Point out leukocytes.
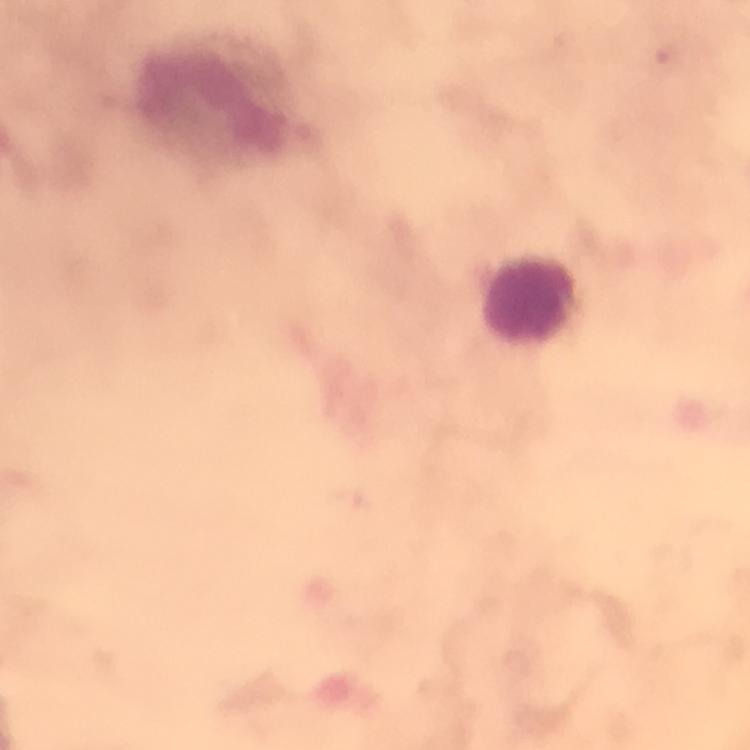

Approximate centers as (x, y) in pixels.
Leukocytes: (216, 103), (530, 301).

Summary:
  - Context: from a diagnostic examination for malaria
  - Plasmodium parasites: none detected
  - Capture: smartphone mounted on the microscope
  - Image size: 750×750 pixels
  - Cropped from: one field of view
  - Preparation: thick smear
  - Magnification: 100x
  - Immersion oil: used
  - Stain: Giemsa